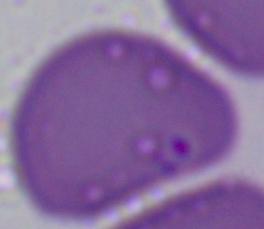

Photomicrograph. 1000x magnification. A Babesia parasite is seen.